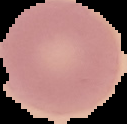 Image is 127×124 pixels. From a thin blood smear. Malaria status: uninfected. Segmented cell region on a black background.